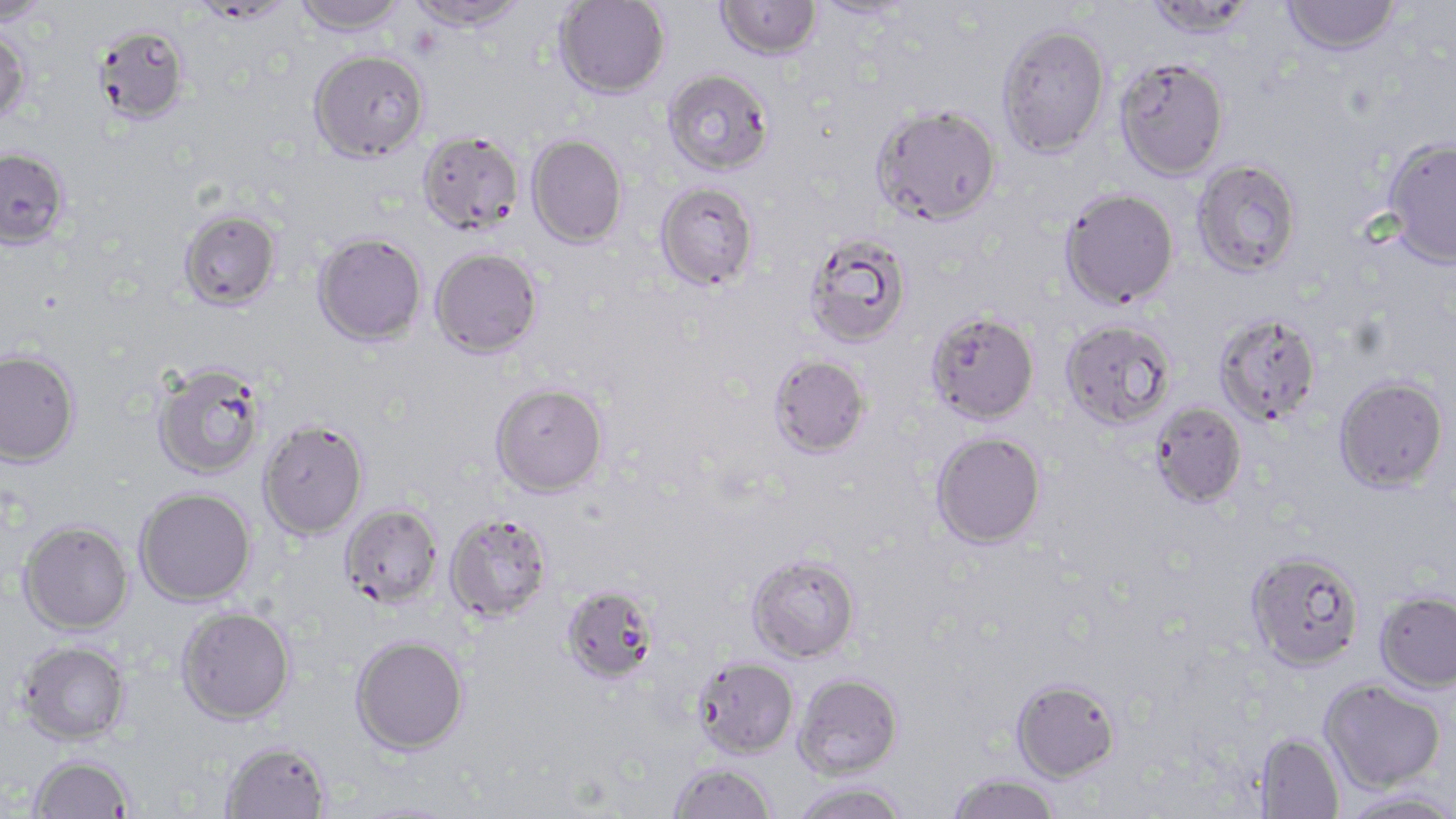 Approximate bounding boxes as [x1, y1, x2, y2] in pixels. Uninfected red blood cell locations: [0, 0, 51, 26], [292, 0, 407, 36], [406, 0, 527, 31], [555, 0, 670, 99], [1143, 0, 1259, 39], [1282, 0, 1401, 56], [194, 1, 294, 24], [717, 1, 821, 60], [809, 1, 917, 22], [93, 22, 191, 125], [996, 23, 1111, 157], [0, 27, 31, 125], [309, 49, 429, 162], [1114, 57, 1230, 180], [663, 69, 773, 176], [872, 104, 1002, 225], [416, 130, 524, 235], [526, 134, 627, 248], [1381, 136, 1456, 269], [0, 147, 70, 250], [1192, 159, 1303, 278], [655, 182, 758, 291], [1060, 187, 1180, 309], [178, 209, 282, 311], [313, 232, 427, 346], [803, 232, 913, 349], [430, 247, 543, 358], [926, 310, 1040, 425], [1212, 311, 1322, 427], [1061, 319, 1177, 430], [0, 348, 81, 467], [768, 354, 871, 459], [151, 361, 266, 479], [1333, 375, 1449, 493], [490, 382, 609, 498], [1149, 402, 1247, 508], [257, 419, 369, 540], [930, 431, 1046, 550], [134, 487, 256, 607], [339, 502, 443, 609], [444, 511, 553, 623], [18, 520, 134, 634], [1245, 550, 1364, 672], [746, 553, 861, 663], [560, 585, 658, 685], [1375, 590, 1456, 693], [176, 606, 296, 725], [350, 635, 469, 755], [17, 640, 131, 745], [693, 657, 799, 759], [793, 673, 904, 779], [1011, 678, 1120, 782], [1321, 678, 1446, 794], [1254, 732, 1344, 818], [220, 740, 331, 819], [29, 754, 135, 818], [668, 761, 778, 819], [946, 774, 1062, 819], [792, 781, 910, 819], [1340, 791, 1456, 819]. Slide-level diagnosis: Plasmodium falciparum. Light microscopy. Single field of view. May-Grünwald-Giemsa-stained preparation. 1000x magnification. Image is 1456×819 pixels. Thin blood smear.